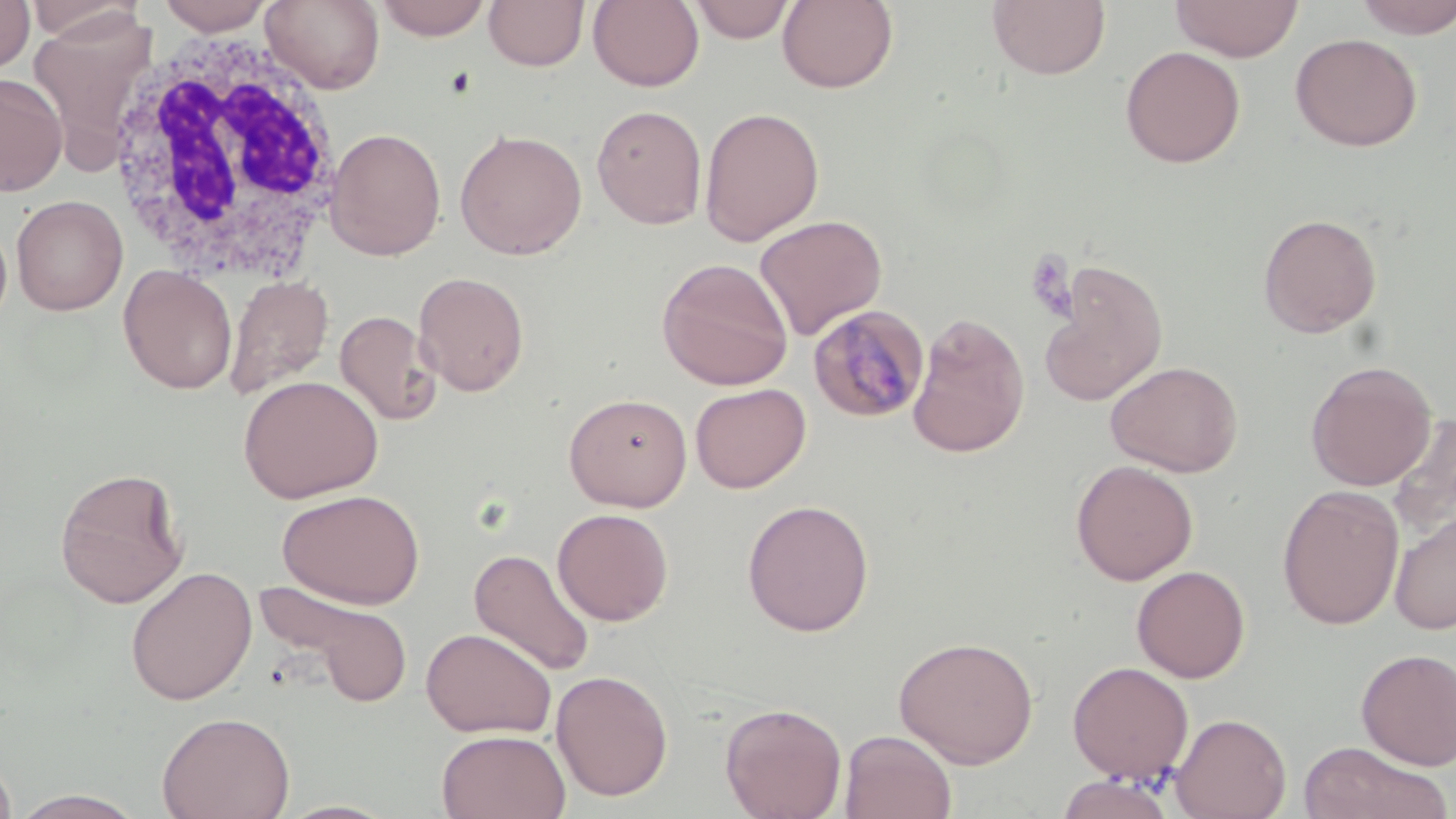 Approximate bounding boxes as (x1, y1, x2, y2) in pixels. Plasmodium malariae-infected red blood cell locations: (808, 304, 931, 423). White blood cell locations: (239, 0, 382, 100), (100, 26, 346, 281). Uninfected red blood cell locations: (0, 0, 34, 73), (22, 0, 144, 44), (156, 0, 275, 34), (261, 0, 385, 94), (374, 0, 493, 40), (484, 0, 589, 71), (588, 0, 705, 91), (689, 0, 795, 43), (777, 0, 898, 93), (987, 0, 1110, 81), (1352, 0, 1456, 39), (1169, 1, 1304, 62), (28, 12, 158, 161), (1290, 32, 1423, 152), (1120, 45, 1246, 168), (0, 73, 67, 197), (591, 104, 708, 229), (699, 106, 824, 247), (324, 126, 447, 261), (454, 128, 588, 260), (11, 195, 127, 315), (1258, 213, 1382, 339), (753, 214, 888, 340), (0, 218, 12, 329), (657, 257, 793, 390), (1040, 261, 1169, 406), (118, 264, 237, 395), (413, 271, 530, 397), (224, 275, 332, 399), (334, 309, 442, 426), (906, 312, 1030, 459), (1105, 360, 1244, 477), (1306, 360, 1436, 491), (238, 374, 384, 503), (690, 383, 810, 493), (564, 392, 693, 511), (1387, 412, 1456, 543), (1071, 460, 1198, 585), (54, 466, 189, 609), (1277, 485, 1404, 630), (277, 489, 425, 609), (742, 499, 874, 637), (552, 508, 674, 625), (1390, 510, 1456, 636), (469, 548, 596, 677), (1131, 564, 1251, 683), (124, 565, 258, 705), (257, 582, 415, 706), (420, 627, 556, 738), (893, 635, 1039, 767), (1355, 648, 1456, 770), (1066, 661, 1194, 784), (551, 669, 673, 801), (720, 702, 847, 819), (157, 711, 295, 819), (1170, 712, 1291, 819), (436, 729, 570, 819), (839, 730, 957, 818), (1297, 740, 1452, 819), (0, 753, 18, 819), (1055, 772, 1179, 818), (10, 789, 147, 818), (276, 800, 399, 819). Slide-level diagnosis: Plasmodium malariae. May-Grünwald-Giemsa-stained preparation. 1000x magnification. Optical microscopy. One field of a larger specimen. Image is 1456×819 pixels. Thin blood film.